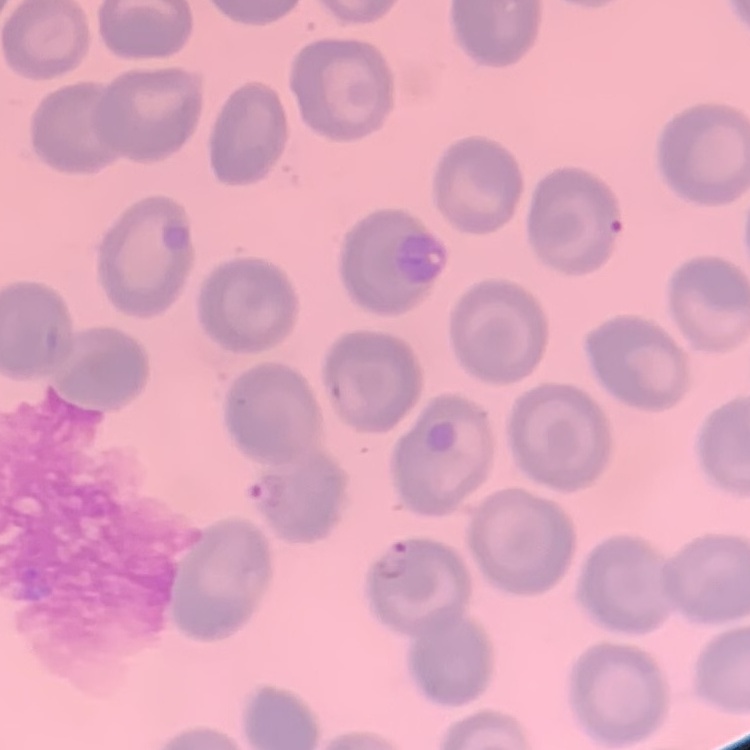
Summary:
  - Red blood cell morphology: no rouleaux formation
  - Stain: Field's or Giemsa
  - Image type: square crop of a larger photomicrograph
  - Preparation: thin blood film